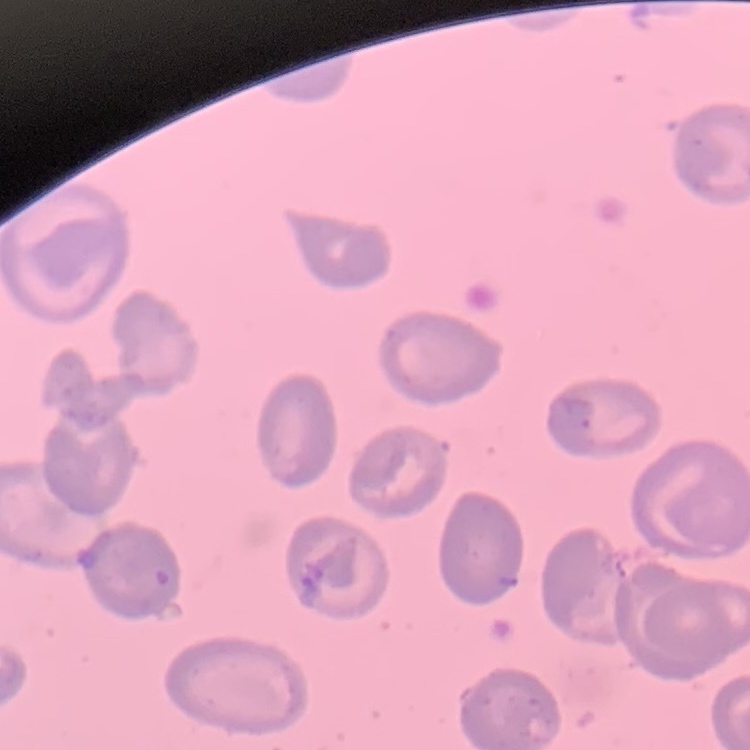

Summary:
  - Erythrocyte morphology: no rouleaux formation
  - Stain: Field's or Giemsa
  - Preparation: thin blood smear
  - Image type: square crop of a larger photomicrograph